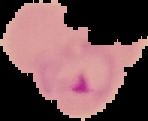
image type = segmented cell region with the area outside set to black
preparation = thin blood smear
image size = 148×121 pixels
malaria status = parasitized